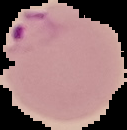
Summary:
  - Preparation: thin blood film
  - Image type: segmented cell region on a black background
  - Result: Plasmodium parasites detected
  - Image size: 127×130 pixels